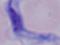
Summary:
  - Magnification: 1000x
  - Identification: trypanosome
  - Modality: micrograph